Draw a bounding box around every artifact (platelet-like body, stain precipitate, or debris).
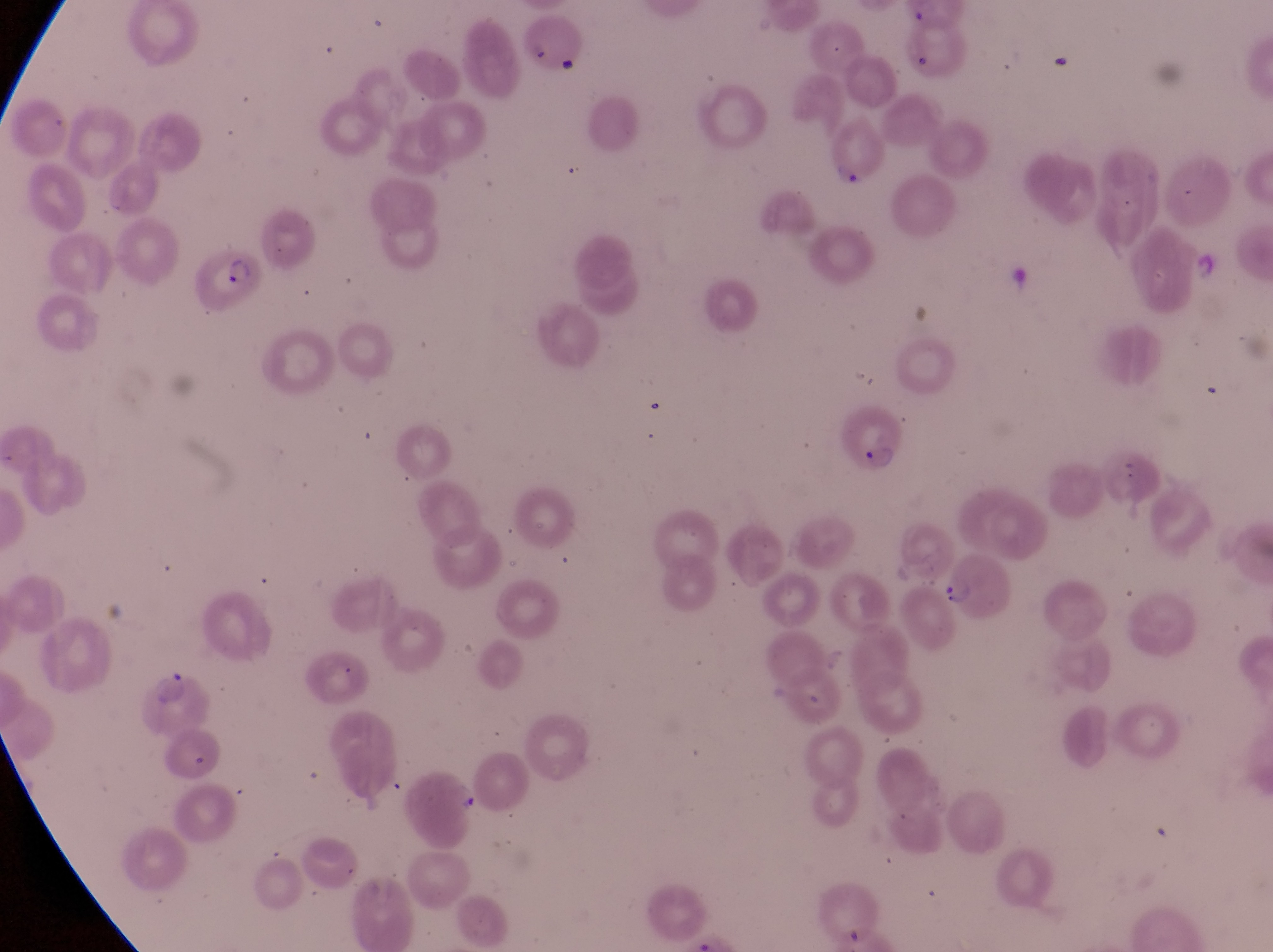
Approximate bounding boxes as [left, top, right, bottom] in pixels.
Artifacts (platelet-like body, stain precipitate, or debris): [447, 782, 482, 819].

Parasitised red blood cell locations: [816, 117, 888, 189], [190, 247, 268, 310], [839, 402, 909, 476], [938, 554, 1016, 619]. Captured by a smartphone held over the eyepiece of an Olympus CX-23 microscope. Image is 1273×952 pixels. Single field of view. Sample from Uganda. Thin blood film. At a magnification of 1000x.